Describe the morphology of the erythrocytes.
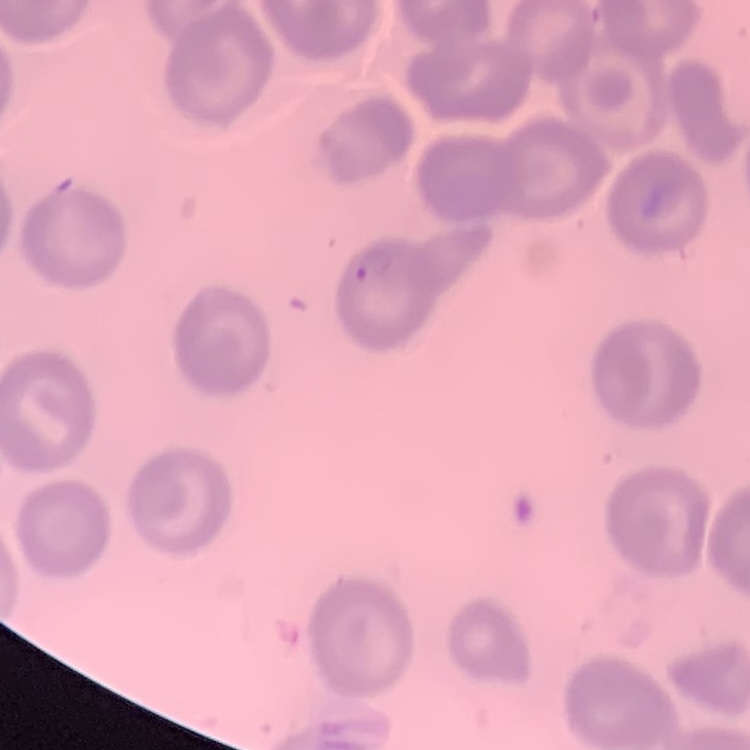

No rouleaux formation.

image type = one tile cut from a larger photomicrograph
preparation = thin blood film
stain = Field's or Giemsa